Give the location of every WBC.
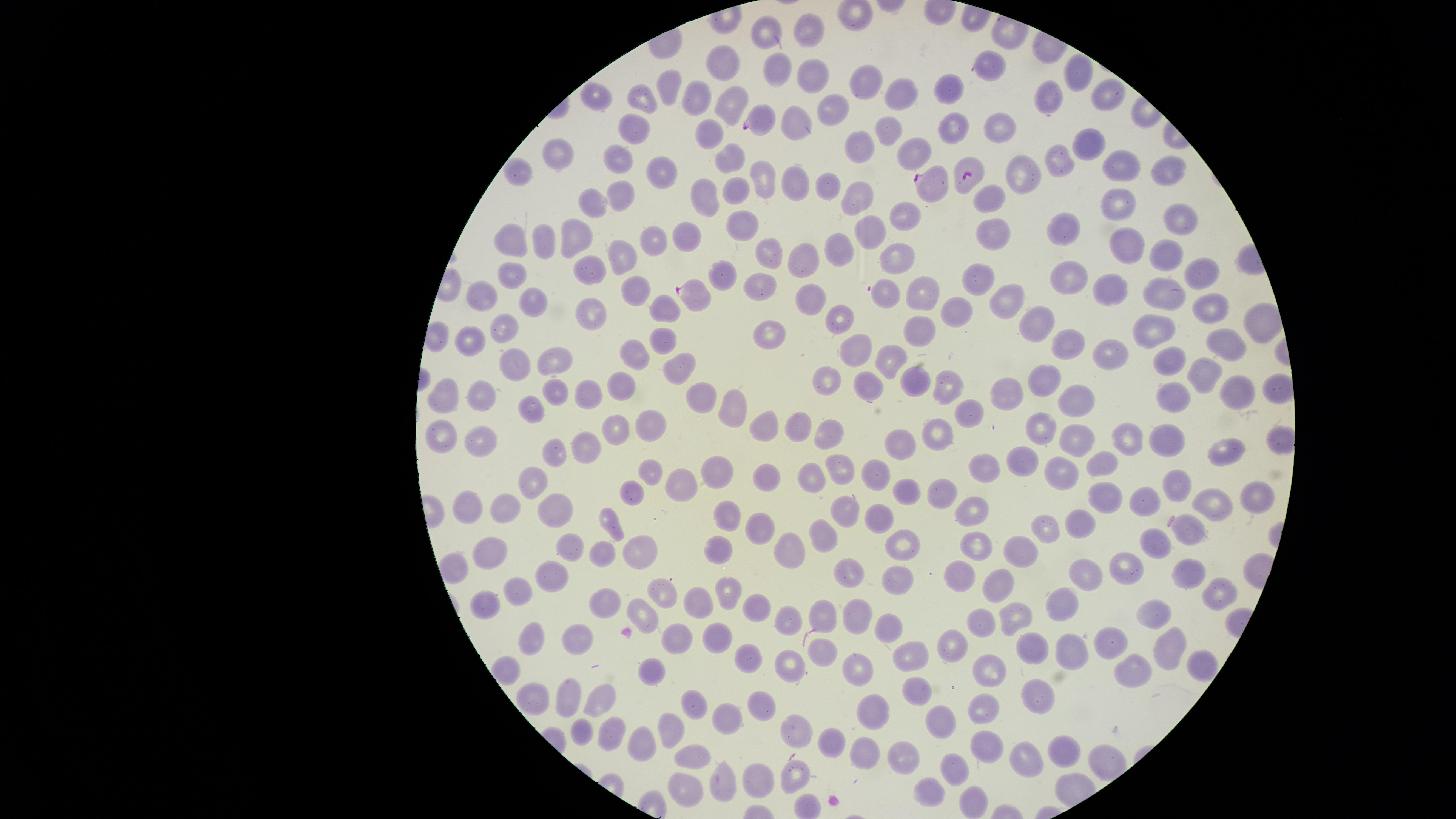

No WBCs identified.

{
  "field_of_view": "single",
  "image_size": "1456×819 pixels",
  "uninfected_RBCs": "approximate marker points as {x, y} in pixels: {808, 29}, {764, 30}, {724, 60}, {991, 67}, {813, 70}, {774, 71}, {1076, 74}, {867, 82}, {670, 87}, {948, 92}, {898, 93}, {598, 96}, {698, 98}, {1107, 98}, {642, 99}, {1051, 103}, {728, 107}, {829, 109}, {792, 121}, {952, 124}, {1002, 124}, {630, 129}, {886, 129}, {712, 132}, {1082, 142}, {861, 146}, {907, 146}, {734, 153}, {562, 157}, {619, 158}, {1058, 161}, {1118, 161}, {1165, 166}, {1017, 172}, {518, 173}, {658, 174}, {760, 179}, {795, 181}, {858, 187}, {827, 188}, {701, 189}, {732, 191}, {618, 195}, {984, 196}, {592, 198}, {1117, 204}, {905, 213}, {1179, 218}, {739, 221}, {871, 229}, {1066, 230}, {989, 231}, {685, 233}, {575, 234}, {509, 238}, {648, 240}, {545, 243}, {839, 247}, {1129, 247}, {771, 252}, {1159, 255}, {801, 257}, {620, 258}, {897, 262}, {588, 268}, {1199, 270}, {724, 273}, {981, 273}, {508, 276}, {1075, 277}, {757, 287}, {886, 290}, {633, 291}, {1110, 291}, {1159, 291}, {480, 294}, {923, 294}, {814, 296}, {999, 300}, {530, 307}, {1214, 309}, {659, 312}, {955, 312}, {594, 315}, {836, 316}, {1038, 316}, {913, 327}, {502, 328}, {1153, 329}, {774, 331}, {468, 341}, {662, 342}, {1219, 343}, {1066, 345}, {632, 350}, {861, 352}, {1115, 354}, {555, 360}, {1161, 360}, {677, 361}, {894, 361}, {508, 364}, {1198, 370}, {1047, 379}, {822, 380}, {864, 381}, {619, 385}, {915, 385}, {946, 385}, {699, 389}, {554, 391}, {1238, 391}, {454, 392}, {594, 392}, {1013, 392}, {1170, 393}, {483, 395}, {1080, 399}, {732, 407}, {533, 411}, {966, 414}, {801, 420}, {764, 424}, {653, 425}, {1040, 427}, {941, 428}, {833, 429}, {612, 430}, {443, 431}, {479, 433}, {1166, 436}, {1132, 438}, {1078, 439}, {581, 441}, {903, 444}, {557, 451}, {1025, 451}, {1225, 451}, {1103, 462}, {988, 463}, {719, 468}, {843, 468}, {1058, 468}, {874, 469}, {652, 470}, {767, 474}, {811, 475}, {540, 478}, {676, 480}, {1176, 485}, {635, 486}, {903, 488}, {942, 491}, {1257, 495}, {1150, 501}, {1114, 503}, {469, 506}, {507, 508}, {1217, 509}, {972, 510}, {731, 513}, {843, 513}, {556, 515}, {878, 515}, {613, 521}, {1046, 523}, {1078, 525}, {760, 530}, {1185, 530}, {820, 539}, {494, 542}, {720, 544}, {787, 544}, {573, 545}, {1154, 546}, {636, 552}, {903, 552}, {602, 553}, {973, 553}, {1020, 555}, {1128, 565}, {454, 570}, {853, 574}, {1191, 574}, {548, 576}, {1082, 576}, {957, 580}, {899, 583}, {996, 583}, {517, 590}, {666, 591}, {723, 591}, {1214, 591}, {1063, 601}, {481, 602}, {607, 603}, {695, 604}, {759, 605}, {640, 611}, {1155, 612}, {855, 614}, {1019, 615}, {820, 619}, {982, 619}, {783, 620}, {891, 625}, {574, 631}, {723, 634}, {676, 635}, {533, 640}, {1034, 642}, {1107, 643}, {956, 645}, {1165, 648}, {1064, 650}, {909, 652}, {820, 655}, {753, 658}, {788, 658}, {1197, 661}, {860, 664}, {992, 667}, {1135, 667}, {508, 670}, {655, 671}, {569, 691}, {913, 691}, {1039, 696}, {539, 701}, {597, 702}, {691, 702}, {759, 706}, {985, 706}, {873, 709}, {728, 716}, {936, 719}, {584, 729}, {610, 730}, {669, 730}, {790, 732}, {986, 738}, {637, 742}, {833, 744}, {1060, 747}, {902, 749}, {692, 752}, {864, 757}, {1027, 758}, {954, 768}, {764, 775}, {797, 780}, {723, 785}, {683, 790}, {930, 794}, {973, 801}",
  "parasitized_RBCs": "approximate marker points as {x, y} in pixels: {759, 120}, {964, 175}, {929, 181}, {695, 292}",
  "species": "Plasmodium falciparum",
  "preparation": "thin blood smear",
  "visible_region": "circular",
  "stain": "Giemsa",
  "capture": "smartphone photograph through the microscope eyepiece",
  "presence": "malaria parasites detected"
}